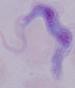
magnification = 1000x
modality = micrograph
identification = trypanosome